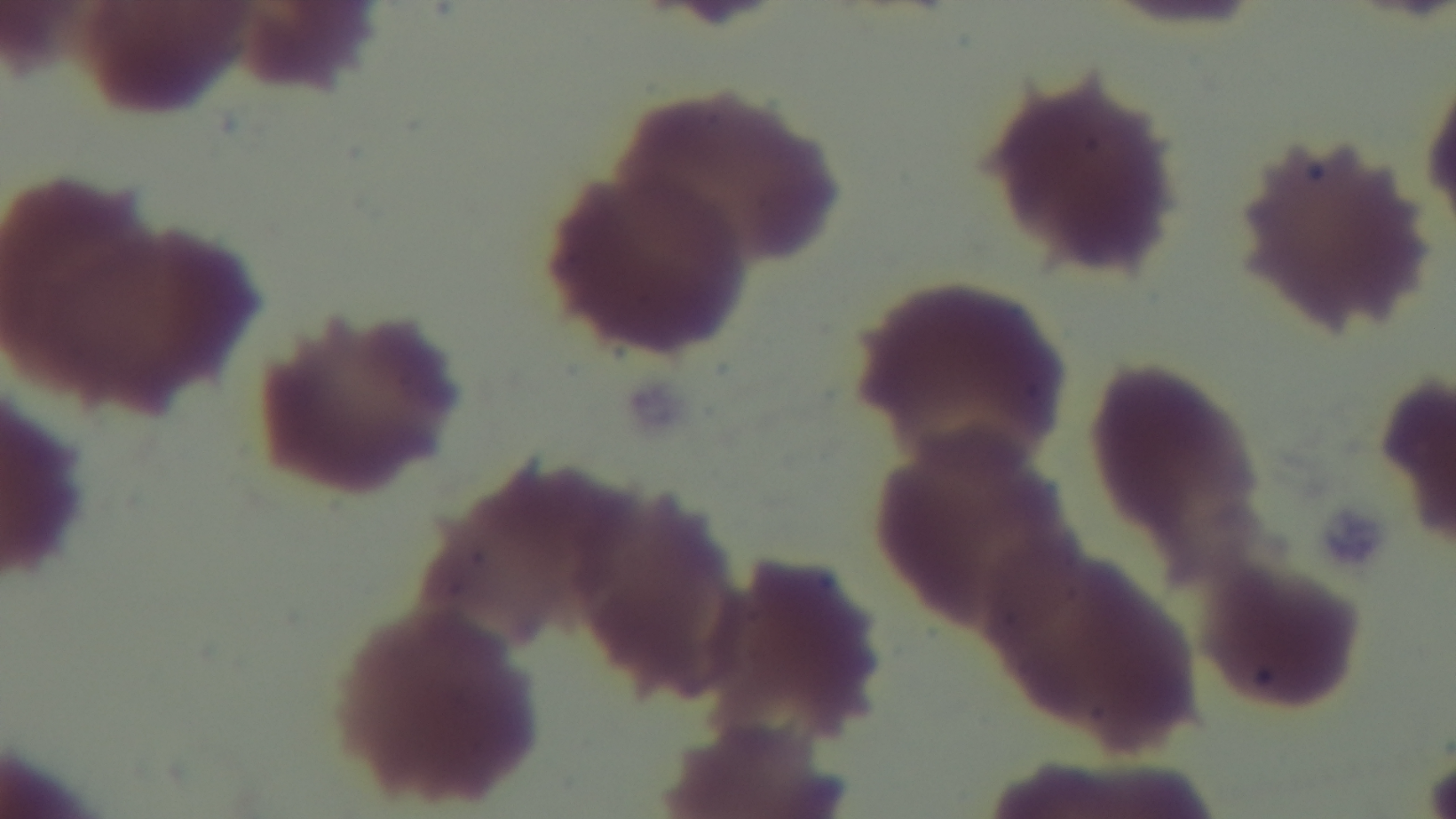

Light microscopy. Preparation: thin. Malaria status: uninfected. Giemsa stain. 100x oil-immersion objective. One field from the slide. Captured with a mounted 4K digital camera.